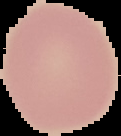

image size = 121×136 pixels
preparation = thin blood smear
result = no Plasmodium parasites detected
image type = cell region segmented out of the field of view; surrounding area masked to black